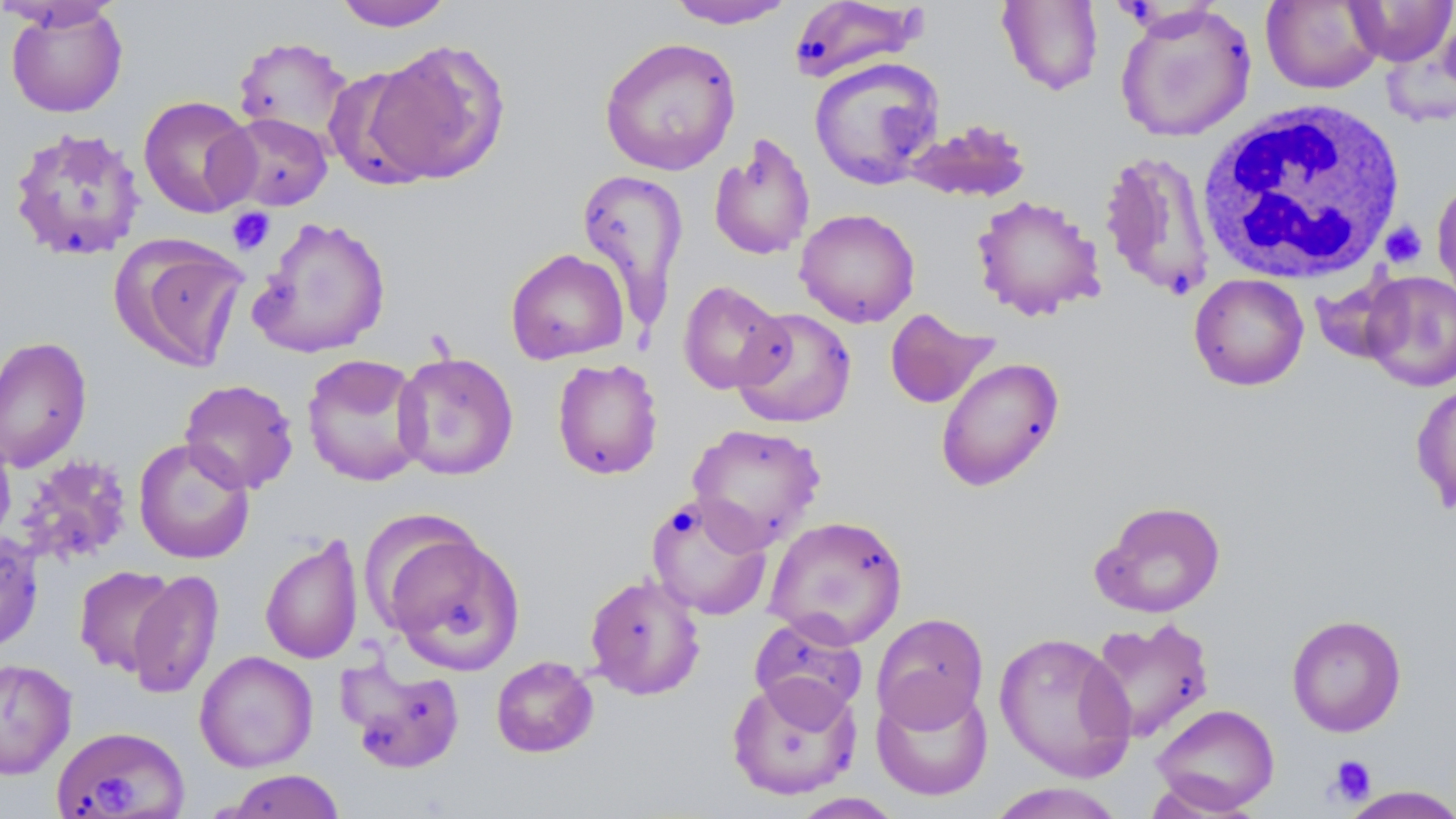
Approximate bounding boxes as (x1, y1, x2, y2) in pixels. White blood cell locations: (1196, 98, 1409, 285). Uninfected red blood cell locations: (332, 0, 457, 31), (665, 0, 796, 29), (787, 0, 926, 83), (0, 1, 124, 30), (997, 1, 1103, 95), (1261, 1, 1383, 94), (1344, 1, 1456, 66), (5, 4, 128, 118), (1115, 4, 1256, 143), (233, 35, 357, 149), (599, 37, 742, 176), (364, 39, 510, 185), (808, 57, 944, 190), (325, 66, 453, 191), (137, 94, 258, 218), (218, 112, 334, 211), (904, 118, 1032, 203), (7, 126, 147, 263), (708, 133, 816, 262), (1097, 149, 1217, 300), (576, 169, 690, 323), (1432, 176, 1456, 311), (971, 194, 1106, 321), (794, 208, 920, 327), (248, 215, 392, 359), (114, 236, 250, 372), (505, 247, 629, 364), (1359, 271, 1456, 391), (1189, 273, 1309, 391), (678, 280, 790, 394), (732, 307, 856, 428), (884, 309, 999, 409), (0, 335, 93, 473), (392, 351, 519, 480), (301, 353, 428, 487), (935, 357, 1065, 492), (552, 358, 664, 480), (1412, 377, 1456, 518), (179, 378, 299, 494), (686, 423, 826, 551), (0, 424, 16, 549), (133, 438, 255, 565), (15, 454, 134, 566), (645, 494, 773, 620), (1091, 499, 1226, 617), (763, 515, 908, 649), (380, 528, 526, 674), (0, 531, 44, 654), (260, 533, 364, 666), (74, 565, 177, 676), (127, 570, 224, 700), (584, 573, 706, 700), (871, 612, 989, 731), (748, 614, 868, 723), (1286, 614, 1407, 737), (1085, 617, 1215, 744), (994, 631, 1137, 782), (194, 650, 319, 772), (490, 655, 599, 758), (0, 658, 76, 779), (338, 658, 467, 774), (726, 674, 862, 801), (871, 682, 993, 801), (1151, 703, 1280, 814), (52, 726, 190, 818), (221, 769, 347, 819), (984, 782, 1130, 819), (1340, 786, 1456, 819), (788, 793, 905, 818). Platelet locations: (227, 207, 275, 255), (1380, 221, 1427, 268), (1327, 754, 1376, 806), (94, 769, 134, 813). Slide-level diagnosis: negative for blood parasites. Thin blood smear. May-Grünwald-Giemsa-stained preparation. 1000x magnification. Image is 1456×819 pixels. Single field of view. Optical microscopy.